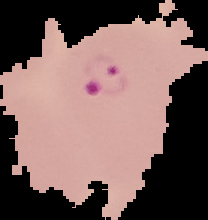

image size = 208×220 pixels
image type = segmented cell region with the area outside set to black
preparation = thin blood film
result = malaria parasites identified